Outline each blood parasite and name the species.
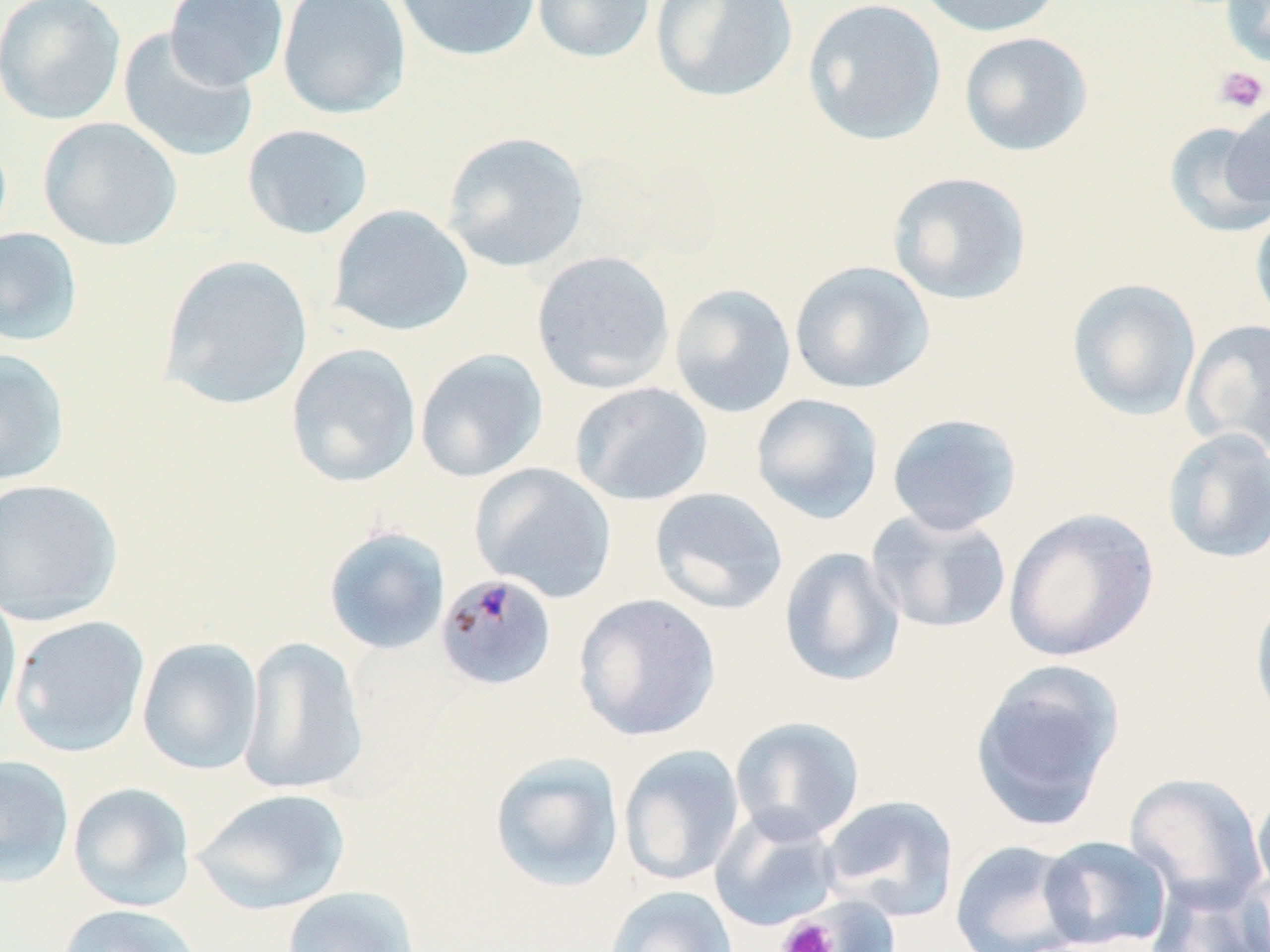

Approximate bounding boxes as [x1, y1, x2, y2] in pixels.
Plasmodium malariae-infected red blood cells: [443, 573, 557, 688].
No Plasmodium falciparum, Plasmodium ovale, Plasmodium vivax, Babesia divergens, or Trypanosoma brucei observed.

slide-level diagnosis = Plasmodium malariae
stain = May-Grünwald-Giemsa
field of view = single
modality = light microscopy
platelet locations = approximate bounding boxes as [x1, y1, x2, y2] in pixels: [1214, 65, 1268, 114], [777, 916, 840, 952]
magnification = 1000x
uninfected red blood cell locations = approximate bounding boxes as [x1, y1, x2, y2] in pixels: [0, 0, 126, 125], [164, 0, 289, 90], [277, 0, 411, 119], [393, 0, 542, 62], [531, 0, 656, 64], [650, 0, 799, 104], [801, 0, 947, 147], [911, 0, 1067, 38], [1220, 0, 1270, 69], [118, 27, 259, 164], [958, 31, 1093, 157], [1225, 100, 1270, 214], [37, 117, 182, 251], [1163, 122, 1270, 238], [241, 123, 375, 240], [441, 131, 590, 273], [887, 171, 1032, 306], [327, 203, 474, 337], [1250, 206, 1270, 331], [0, 228, 84, 347], [531, 251, 675, 394], [158, 254, 313, 410], [789, 260, 935, 395], [1066, 278, 1202, 422], [669, 283, 797, 418], [1182, 318, 1270, 457], [285, 343, 422, 488], [0, 349, 71, 487], [415, 349, 548, 483], [570, 381, 713, 506], [750, 393, 884, 524], [886, 412, 1023, 536], [1161, 427, 1270, 565], [470, 463, 617, 603], [0, 477, 124, 626], [650, 487, 788, 615], [1003, 506, 1160, 663], [866, 509, 1012, 635], [322, 526, 451, 656], [778, 546, 907, 687], [1249, 587, 1270, 730], [0, 589, 22, 735], [573, 593, 721, 742], [9, 615, 150, 757], [239, 636, 369, 797], [136, 637, 263, 775], [969, 659, 1125, 832], [729, 715, 866, 844], [619, 745, 745, 887], [488, 752, 625, 893], [0, 753, 75, 888], [1124, 771, 1267, 910], [68, 781, 196, 912], [1252, 783, 1270, 902], [191, 787, 352, 915], [820, 794, 959, 922], [710, 809, 842, 932], [1038, 834, 1174, 950], [949, 839, 1089, 952], [1235, 868, 1270, 951], [1145, 878, 1270, 952], [605, 884, 738, 952], [281, 885, 421, 952], [774, 895, 897, 952], [58, 903, 204, 952]
preparation = thin blood smear
image size = 1270×952 pixels